Locate and identify every blood parasite.
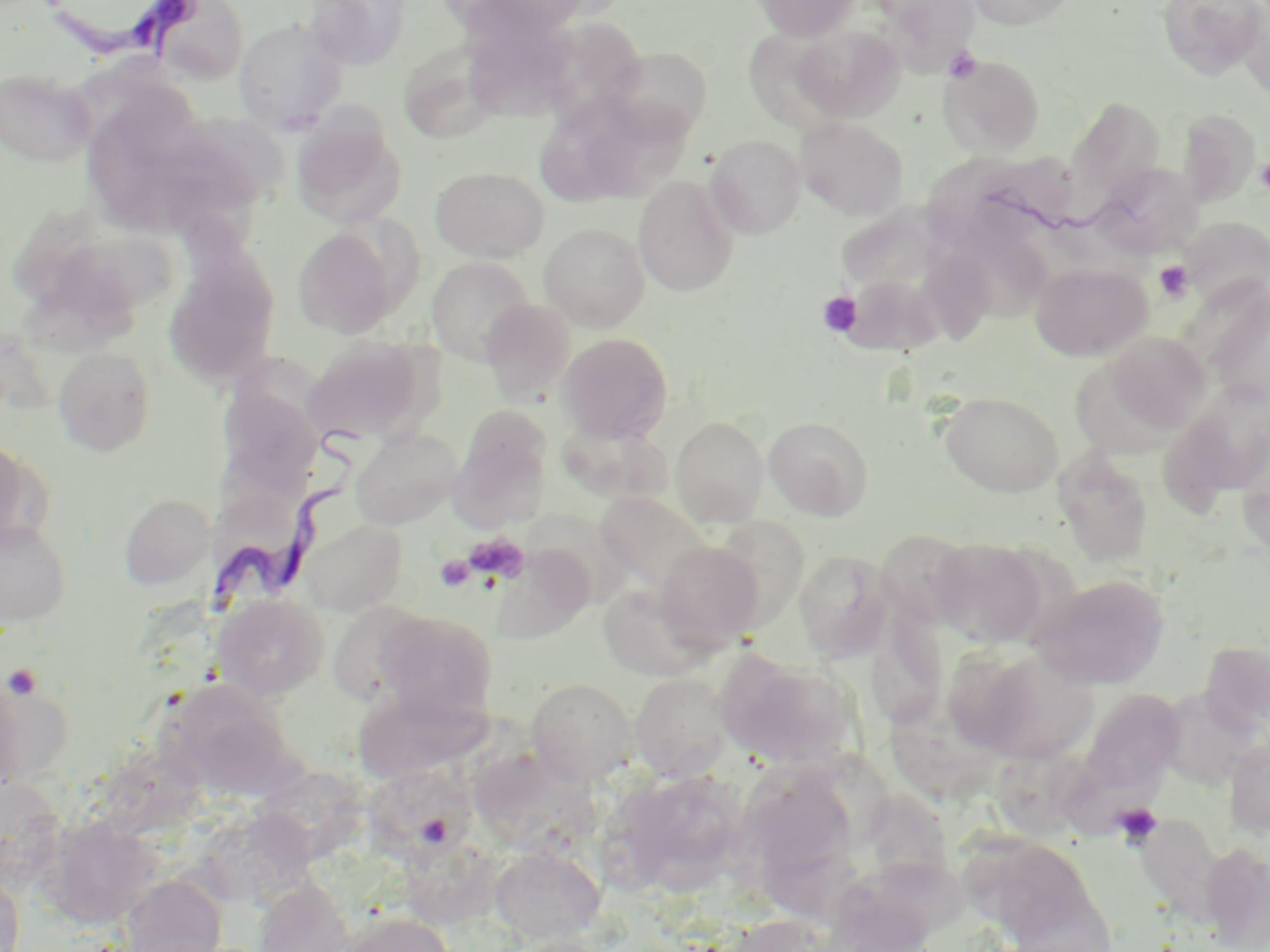
Approximate bounding boxes as [x1, y1, x2, y2] in pixels.
Trypanosoma brucei: [39, 1, 206, 64], [208, 427, 375, 623].
No Plasmodium falciparum, Plasmodium ovale, Plasmodium malariae, Plasmodium vivax, or Babesia divergens observed.

Uninfected red blood cell locations: [304, 0, 411, 70], [464, 0, 598, 36], [750, 0, 862, 41], [872, 0, 981, 71], [965, 0, 1076, 30], [1158, 0, 1268, 79], [149, 1, 248, 84], [1237, 5, 1270, 101], [232, 18, 346, 134], [469, 20, 586, 124], [789, 25, 905, 122], [741, 30, 846, 133], [397, 42, 503, 145], [602, 46, 712, 144], [941, 54, 1046, 158], [0, 68, 96, 167], [540, 90, 643, 204], [1066, 96, 1165, 203], [589, 104, 698, 204], [291, 105, 406, 228], [1177, 107, 1261, 208], [796, 117, 907, 220], [706, 134, 806, 238], [163, 137, 268, 226], [972, 152, 1079, 228], [927, 153, 1031, 259], [1092, 163, 1203, 258], [431, 166, 550, 262], [632, 175, 739, 297], [1182, 217, 1270, 308], [841, 221, 948, 292], [539, 223, 650, 332], [291, 226, 403, 339], [962, 227, 1050, 324], [51, 238, 185, 312], [163, 249, 280, 388], [427, 256, 535, 365], [1031, 263, 1152, 361], [839, 273, 948, 358], [1205, 283, 1270, 408], [481, 299, 575, 404], [1102, 331, 1211, 438], [557, 332, 673, 442], [302, 336, 429, 444], [53, 346, 156, 457], [219, 367, 320, 487], [1159, 390, 1267, 510], [940, 391, 1062, 497], [451, 408, 554, 528], [671, 415, 770, 527], [764, 416, 874, 521], [350, 428, 464, 530], [0, 440, 40, 550], [1052, 448, 1154, 567], [595, 492, 712, 594], [119, 493, 215, 590], [0, 518, 73, 627], [302, 519, 406, 616], [875, 529, 976, 627], [929, 538, 1049, 647], [653, 540, 764, 650], [493, 544, 595, 644], [793, 548, 894, 663], [1033, 573, 1171, 690], [597, 582, 714, 681], [211, 593, 329, 700], [326, 603, 433, 706], [374, 610, 499, 720], [873, 619, 951, 728], [1199, 640, 1269, 735], [960, 644, 1100, 763], [718, 652, 859, 773], [629, 672, 733, 781], [0, 674, 25, 800], [160, 678, 300, 801], [526, 678, 639, 785], [351, 684, 485, 783], [1081, 689, 1185, 793], [882, 692, 1004, 811], [1223, 737, 1270, 838], [1047, 757, 1180, 838], [483, 760, 615, 849], [363, 764, 474, 855], [736, 766, 862, 893], [611, 767, 749, 895], [252, 768, 368, 868], [0, 776, 66, 891], [864, 783, 958, 894], [195, 807, 313, 911], [1135, 811, 1224, 917], [40, 814, 158, 929], [1159, 818, 1258, 944], [958, 823, 1085, 934], [1198, 841, 1270, 950], [489, 844, 606, 944], [839, 858, 979, 949], [994, 872, 1119, 950], [120, 873, 227, 952], [0, 874, 25, 952], [253, 877, 355, 952], [334, 912, 455, 952], [722, 914, 842, 952], [500, 935, 615, 952]. Platelet locations: [943, 45, 982, 83], [1256, 157, 1270, 193], [1155, 261, 1193, 301], [818, 291, 863, 337], [463, 532, 530, 584], [435, 554, 476, 592], [3, 664, 43, 700], [1112, 803, 1163, 849]. Slide-level diagnosis: Trypanosoma brucei. 1000x magnification. May-Grünwald-Giemsa-stained preparation. Single field of view. Image is 1270×952 pixels. Light microscopy. Thin blood film.